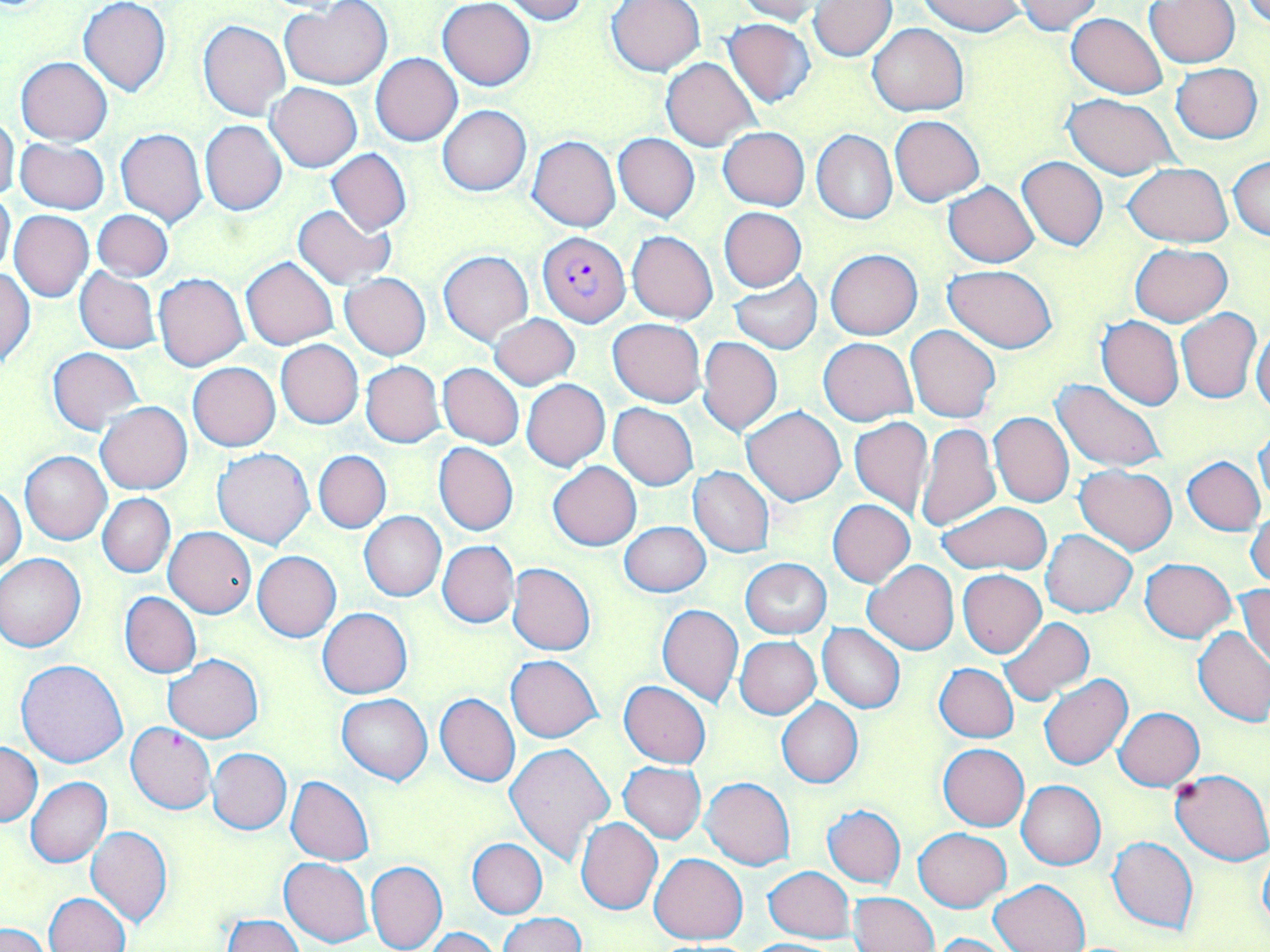
Summary:
  - Coordinate format: approximate bounding boxes as [x1, y1, x2, y2] in pixels
  - Uninfected red blood cell locations: [280, 0, 392, 90], [438, 0, 535, 90], [500, 0, 588, 23], [734, 0, 828, 24], [919, 0, 1027, 35], [1015, 0, 1104, 33], [1146, 0, 1239, 67], [1242, 0, 1270, 28], [79, 1, 170, 96], [605, 1, 707, 77], [808, 1, 896, 60], [1067, 12, 1167, 99], [198, 19, 291, 121], [723, 19, 818, 108], [867, 22, 969, 115], [371, 53, 462, 146], [16, 57, 112, 145], [661, 57, 759, 151], [1171, 63, 1263, 143], [266, 82, 362, 172], [1064, 94, 1179, 180], [438, 105, 531, 195], [890, 115, 984, 205], [0, 116, 20, 202], [200, 120, 286, 216], [719, 127, 810, 211], [116, 128, 207, 227], [813, 130, 897, 224], [613, 133, 699, 222], [528, 136, 621, 232], [16, 138, 108, 215], [327, 148, 411, 235], [1229, 155, 1270, 241], [1017, 156, 1108, 250], [1123, 161, 1233, 246], [943, 182, 1039, 268], [0, 190, 14, 281], [292, 204, 396, 290], [719, 207, 808, 292], [10, 209, 94, 302], [93, 210, 172, 280], [628, 232, 717, 323], [1131, 243, 1231, 325], [439, 249, 532, 344], [826, 249, 922, 340], [241, 257, 338, 350], [945, 264, 1057, 353], [74, 267, 160, 353], [1, 268, 35, 367], [153, 273, 250, 372], [341, 273, 430, 360], [729, 273, 822, 354], [1176, 307, 1262, 404], [489, 314, 581, 391], [1097, 315, 1184, 410], [607, 318, 706, 406], [906, 325, 1002, 423], [1251, 328, 1270, 415], [698, 336, 782, 436], [819, 338, 917, 424], [276, 339, 363, 429], [48, 348, 143, 435], [190, 353, 363, 440], [361, 361, 445, 447], [188, 362, 280, 451], [438, 363, 524, 449], [1052, 379, 1165, 473], [522, 380, 611, 471], [95, 402, 192, 494], [608, 403, 698, 490], [742, 407, 845, 506], [989, 411, 1074, 508], [849, 417, 934, 518], [918, 423, 1000, 532], [1254, 427, 1270, 506], [433, 442, 518, 535], [213, 447, 314, 549], [20, 451, 112, 544], [314, 451, 390, 533], [1184, 457, 1265, 534], [548, 461, 641, 550], [1076, 464, 1177, 554], [689, 467, 774, 557], [0, 486, 26, 574], [98, 494, 175, 577], [828, 499, 915, 588], [936, 501, 1051, 574], [1247, 507, 1270, 591], [359, 511, 446, 601], [619, 523, 711, 596], [164, 527, 256, 618], [1041, 530, 1137, 617], [438, 541, 518, 627], [253, 551, 340, 642], [0, 554, 86, 651], [740, 558, 832, 639], [1139, 559, 1236, 642], [863, 560, 959, 654], [507, 563, 595, 655], [958, 569, 1047, 658], [1237, 582, 1270, 670], [120, 592, 202, 678], [657, 604, 743, 705], [318, 607, 412, 698], [997, 618, 1095, 707], [818, 624, 905, 714], [1194, 626, 1270, 726], [735, 637, 822, 720], [163, 653, 263, 742], [506, 654, 602, 742], [16, 659, 128, 767], [934, 663, 1018, 742], [1040, 674, 1132, 770], [619, 681, 712, 768], [435, 693, 521, 787], [337, 694, 431, 784], [777, 698, 863, 788], [1114, 707, 1205, 790], [126, 722, 216, 814], [1, 743, 42, 825], [506, 743, 615, 863], [937, 744, 1030, 831], [208, 748, 291, 834], [618, 762, 706, 844], [1172, 769, 1270, 865], [286, 776, 375, 865], [26, 777, 112, 867], [701, 777, 796, 870], [1016, 780, 1106, 869], [824, 804, 906, 888], [575, 818, 663, 916], [86, 826, 173, 927], [913, 828, 1011, 911], [1107, 836, 1198, 934], [467, 839, 547, 918], [1257, 845, 1269, 933], [648, 853, 747, 944], [280, 856, 374, 947], [366, 860, 447, 952], [763, 866, 855, 942], [990, 878, 1090, 952], [849, 892, 938, 952], [44, 893, 130, 952], [499, 913, 585, 952], [221, 914, 304, 952], [2, 924, 53, 952], [426, 927, 501, 952], [928, 932, 1021, 952], [742, 939, 847, 952]
  - Plasmodium falciparum-infected red blood cell locations: [538, 231, 629, 326]
  - Slide-level diagnosis: Plasmodium falciparum
  - Magnification: 1000x
  - Preparation: thin blood smear
  - Image size: 1270×952 pixels
  - Field of view: one of a larger specimen
  - Modality: optical microscopy
  - Stain: May-Grünwald-Giemsa